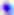
Toxoplasma gondii is seen. Micrograph. 400x magnification.